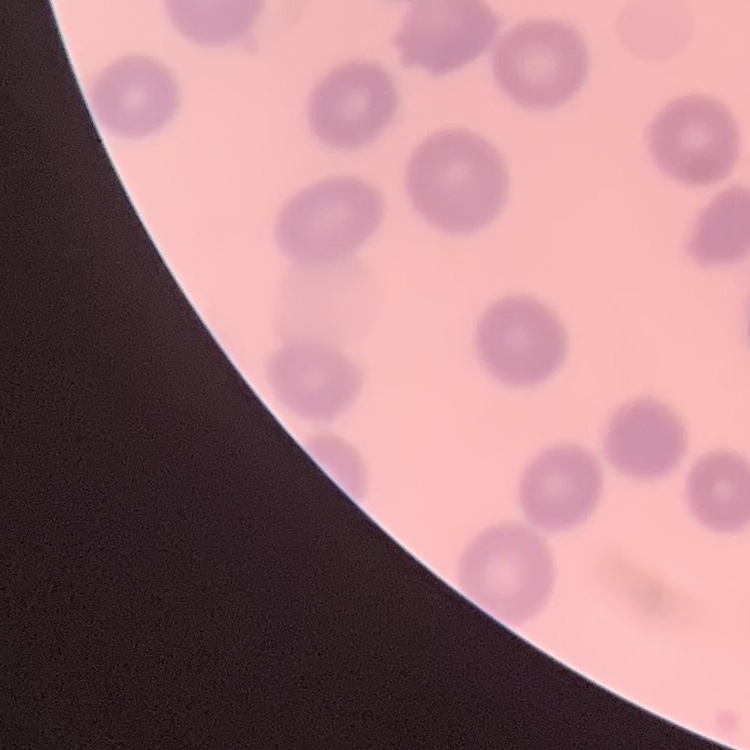 The red blood cells show no rouleaux formation. Square crop of a larger photomicrograph. Stained with either Field's or Giemsa. Thin blood smear.